Give the extent of all Babesia divergens-infected red blood cells.
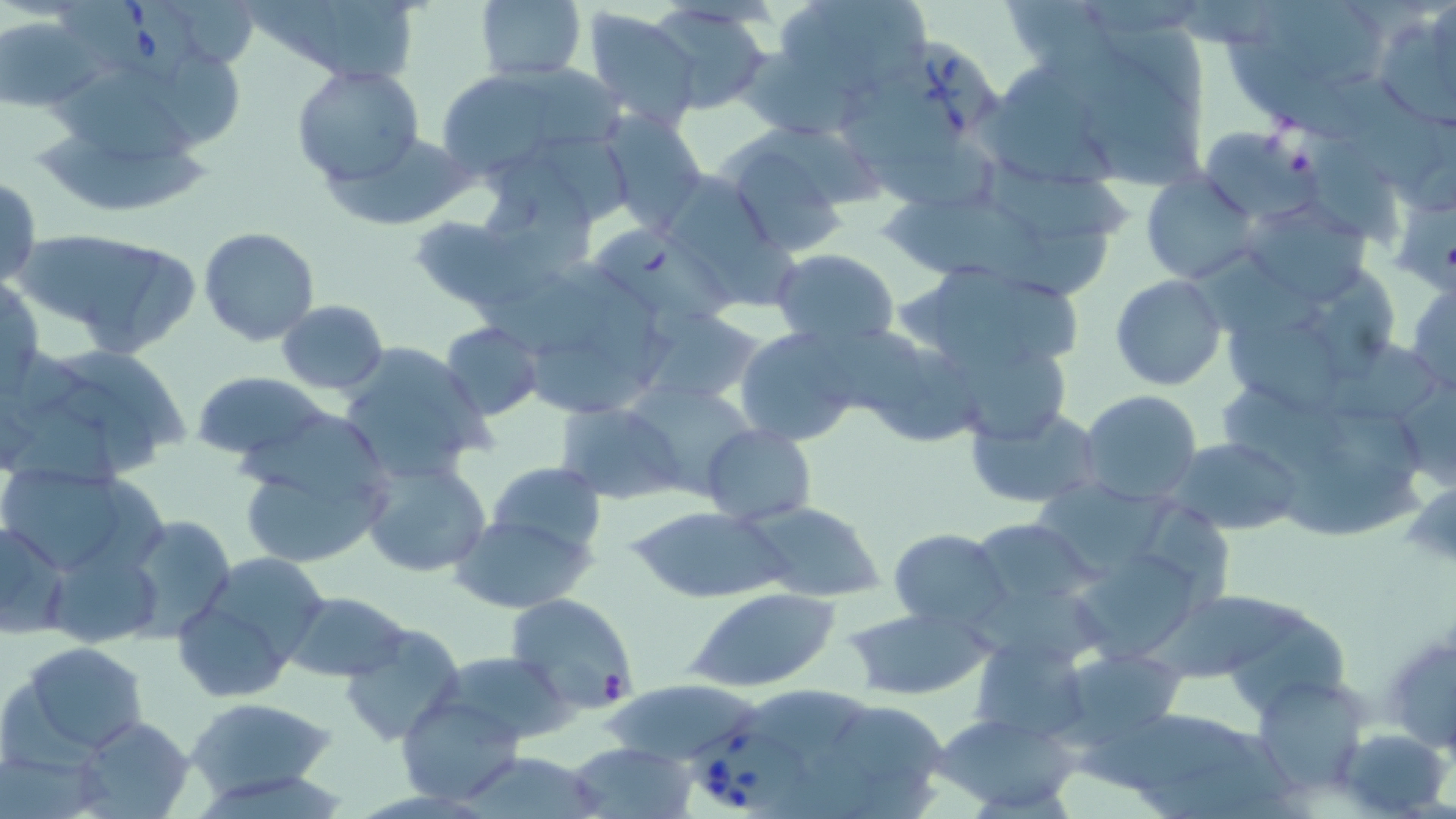

Approximate bounding boxes as named x1/y1/x2/y2 corners in pixels.
Babesia divergens-infected red blood cells: (x1=58, y1=2, x2=204, y2=85), (x1=879, y1=33, x2=1001, y2=149), (x1=686, y1=725, x2=815, y2=810).

Uninfected red blood cell locations: (x1=169, y1=0, x2=255, y2=65), (x1=257, y1=0, x2=422, y2=84), (x1=476, y1=0, x2=586, y2=84), (x1=775, y1=0, x2=933, y2=98), (x1=998, y1=0, x2=1129, y2=81), (x1=1267, y1=2, x2=1378, y2=77), (x1=652, y1=5, x2=771, y2=114), (x1=583, y1=7, x2=700, y2=130), (x1=1373, y1=8, x2=1454, y2=131), (x1=1, y1=14, x2=97, y2=114), (x1=1108, y1=16, x2=1210, y2=113), (x1=1225, y1=33, x2=1350, y2=137), (x1=155, y1=50, x2=245, y2=146), (x1=744, y1=54, x2=867, y2=138), (x1=291, y1=64, x2=425, y2=186), (x1=430, y1=65, x2=618, y2=181), (x1=59, y1=69, x2=198, y2=159), (x1=1339, y1=73, x2=1456, y2=190), (x1=1090, y1=84, x2=1207, y2=188), (x1=834, y1=86, x2=964, y2=168), (x1=983, y1=102, x2=1117, y2=190), (x1=597, y1=111, x2=707, y2=231), (x1=721, y1=122, x2=885, y2=205), (x1=37, y1=124, x2=221, y2=207), (x1=1199, y1=126, x2=1315, y2=223), (x1=325, y1=131, x2=473, y2=232), (x1=493, y1=131, x2=638, y2=217), (x1=718, y1=132, x2=861, y2=259), (x1=1300, y1=137, x2=1397, y2=238), (x1=864, y1=142, x2=1006, y2=212), (x1=988, y1=157, x2=1135, y2=239), (x1=488, y1=163, x2=595, y2=273), (x1=1141, y1=171, x2=1262, y2=285), (x1=0, y1=177, x2=42, y2=290), (x1=675, y1=179, x2=795, y2=308), (x1=874, y1=189, x2=1055, y2=286), (x1=1238, y1=200, x2=1373, y2=306), (x1=1395, y1=203, x2=1456, y2=292), (x1=412, y1=217, x2=524, y2=308), (x1=594, y1=223, x2=740, y2=318), (x1=198, y1=228, x2=320, y2=346), (x1=1025, y1=228, x2=1110, y2=302), (x1=28, y1=230, x2=202, y2=356), (x1=771, y1=248, x2=900, y2=347), (x1=932, y1=264, x2=1026, y2=360), (x1=1315, y1=269, x2=1397, y2=378), (x1=477, y1=273, x2=611, y2=357), (x1=1, y1=275, x2=44, y2=391), (x1=1111, y1=275, x2=1226, y2=391), (x1=1009, y1=280, x2=1082, y2=364), (x1=1405, y1=281, x2=1456, y2=396), (x1=276, y1=300, x2=390, y2=395), (x1=639, y1=307, x2=766, y2=409), (x1=1226, y1=312, x2=1351, y2=423), (x1=440, y1=322, x2=543, y2=420), (x1=734, y1=324, x2=862, y2=446), (x1=534, y1=326, x2=681, y2=416), (x1=847, y1=331, x2=988, y2=448), (x1=337, y1=342, x2=494, y2=485), (x1=1335, y1=342, x2=1443, y2=419), (x1=7, y1=343, x2=193, y2=483), (x1=955, y1=345, x2=1077, y2=444), (x1=1392, y1=365, x2=1456, y2=494), (x1=190, y1=372, x2=333, y2=465), (x1=623, y1=379, x2=758, y2=493), (x1=1216, y1=387, x2=1346, y2=466), (x1=1079, y1=391, x2=1203, y2=504), (x1=556, y1=400, x2=686, y2=504), (x1=966, y1=403, x2=1105, y2=509), (x1=1327, y1=411, x2=1426, y2=483), (x1=235, y1=413, x2=395, y2=569), (x1=700, y1=423, x2=814, y2=525), (x1=1168, y1=438, x2=1304, y2=535), (x1=1284, y1=453, x2=1432, y2=537), (x1=359, y1=457, x2=493, y2=578), (x1=487, y1=461, x2=607, y2=558), (x1=0, y1=462, x2=167, y2=583), (x1=1036, y1=479, x2=1175, y2=570), (x1=1406, y1=488, x2=1456, y2=567), (x1=1146, y1=501, x2=1237, y2=608), (x1=747, y1=502, x2=886, y2=602), (x1=627, y1=505, x2=789, y2=602), (x1=116, y1=513, x2=237, y2=639), (x1=453, y1=515, x2=594, y2=613), (x1=1, y1=521, x2=71, y2=639), (x1=973, y1=523, x2=1109, y2=597), (x1=889, y1=528, x2=1011, y2=631), (x1=1075, y1=544, x2=1198, y2=663), (x1=174, y1=560, x2=328, y2=702), (x1=685, y1=586, x2=841, y2=692), (x1=958, y1=586, x2=1121, y2=660), (x1=1146, y1=586, x2=1308, y2=677), (x1=286, y1=591, x2=413, y2=683), (x1=504, y1=593, x2=636, y2=713), (x1=844, y1=606, x2=994, y2=699), (x1=1231, y1=620, x2=1354, y2=709), (x1=338, y1=622, x2=464, y2=745), (x1=970, y1=636, x2=1092, y2=743), (x1=19, y1=641, x2=149, y2=753), (x1=1054, y1=644, x2=1189, y2=752), (x1=1393, y1=644, x2=1456, y2=751), (x1=436, y1=650, x2=571, y2=745), (x1=1255, y1=673, x2=1370, y2=793), (x1=598, y1=679, x2=767, y2=767), (x1=737, y1=687, x2=866, y2=745), (x1=395, y1=694, x2=523, y2=804), (x1=186, y1=696, x2=337, y2=800), (x1=830, y1=700, x2=944, y2=783), (x1=1102, y1=707, x2=1291, y2=817), (x1=932, y1=711, x2=1080, y2=813), (x1=69, y1=714, x2=197, y2=819), (x1=1338, y1=727, x2=1450, y2=816), (x1=566, y1=743, x2=695, y2=818), (x1=785, y1=745, x2=883, y2=819). Slide-level diagnosis: Babesia divergens. Light microscopy. Single field of view. May-Grünwald-Giemsa-stained preparation. Thin blood film. Captured at 1000x magnification. Image is 1456×819 pixels.